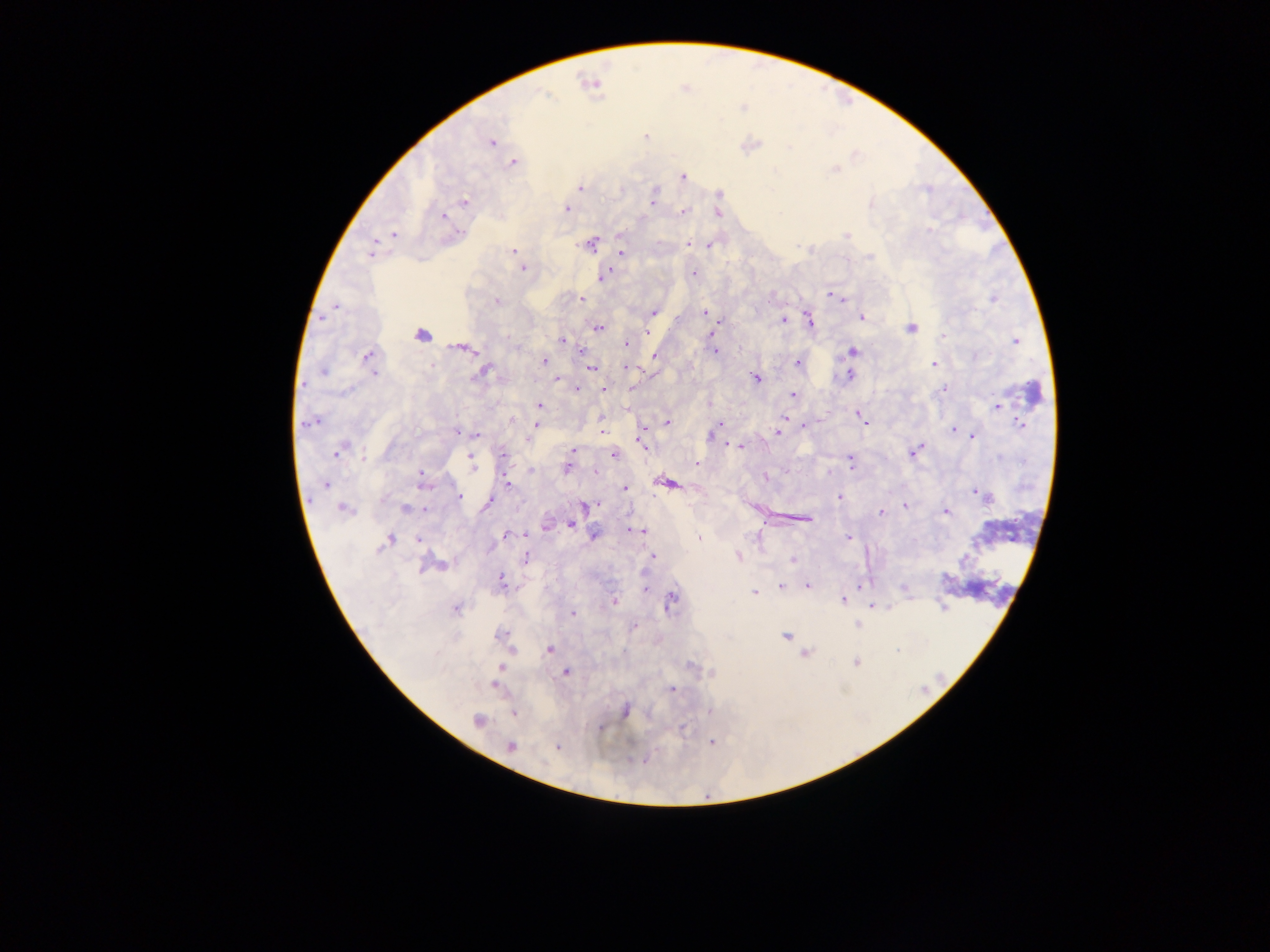

Approximate centers as (x, y) in pixels.
Summary:
  - Plasmodium parasite locations: (545, 94), (743, 107), (646, 136), (491, 143), (513, 163), (835, 169), (683, 176), (580, 188), (719, 194), (653, 200), (464, 202), (871, 204), (566, 209), (683, 212), (719, 214), (443, 216), (929, 230), (394, 235), (619, 235), (847, 236), (689, 244), (591, 245), (709, 245), (512, 251), (372, 253), (622, 253), (522, 268), (693, 274), (603, 276), (829, 295), (581, 298), (992, 298), (842, 299), (496, 302), (335, 306), (653, 312), (704, 312), (861, 317), (783, 319), (719, 320), (810, 321), (598, 327), (911, 327), (646, 332), (711, 334), (421, 336), (943, 336), (561, 340), (1015, 341), (625, 344), (465, 349), (582, 350), (716, 351), (853, 351), (654, 355), (367, 356), (544, 361), (797, 363), (934, 364), (591, 368), (625, 368), (484, 371), (322, 372), (374, 374), (849, 375), (757, 378), (557, 379), (578, 388), (603, 389), (943, 389), (792, 395), (540, 406), (998, 406), (787, 413), (859, 415), (512, 419), (784, 419), (867, 421), (667, 422), (309, 423), (719, 423), (537, 425), (1020, 425), (805, 427), (953, 429), (643, 430), (602, 432), (777, 432), (458, 433), (476, 435), (710, 436), (972, 437), (528, 440), (643, 442), (728, 444), (740, 447), (341, 449), (574, 449), (914, 452), (337, 453), (613, 455), (503, 456), (362, 457), (471, 460), (851, 460), (697, 464), (472, 465), (567, 467), (531, 471), (596, 471), (831, 472), (420, 474), (766, 477), (508, 482), (668, 483), (326, 484), (423, 484), (625, 488), (978, 493), (459, 496), (839, 496), (984, 496), (488, 502), (598, 504), (584, 505), (905, 506), (405, 508), (344, 509), (425, 510), (947, 512), (881, 513), (807, 520), (571, 524), (546, 526), (635, 530), (594, 534), (505, 536), (698, 538), (848, 538), (389, 540), (418, 540), (738, 556), (652, 557), (525, 559), (792, 560), (501, 581), (807, 586), (781, 587), (903, 588), (646, 589), (754, 592), (671, 599), (843, 601), (614, 602), (871, 606), (456, 609), (573, 614), (858, 625), (635, 627), (500, 634), (785, 636), (550, 649), (805, 654), (856, 663), (501, 667), (566, 672), (494, 685), (672, 690), (625, 711), (709, 711), (514, 714), (477, 720), (599, 728), (712, 743), (511, 746), (557, 747)
  - Country: Ghana
  - Capture: mobile-phone photograph through a microscope
  - Field of view: single
  - Image size: 1270×952 pixels
  - Preparation: thick blood film